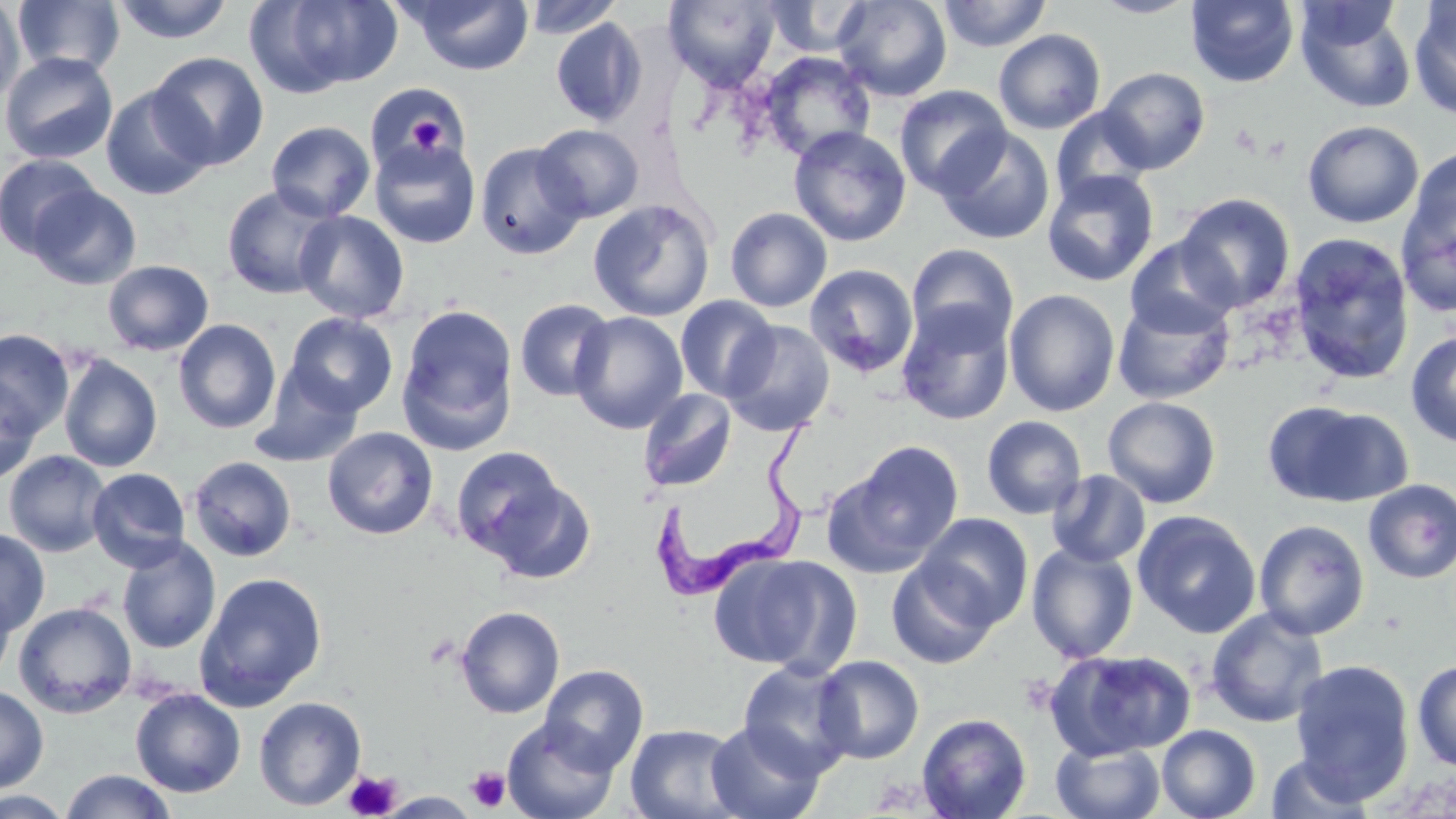

Approximate bounding boxes as (x1,y1)-(x2,y2) corner pairs in pixels. Uninfected red blood cell locations: (112,0)-(235,45), (248,0)-(403,95), (404,0)-(535,76), (522,0)-(623,39), (663,0)-(781,90), (763,0)-(874,58), (833,0)-(952,102), (937,0)-(1052,52), (1090,0)-(1198,18), (1186,0)-(1299,87), (0,1)-(26,106), (13,1)-(125,78), (1409,2)-(1456,121), (1295,3)-(1417,113), (550,17)-(648,127), (993,29)-(1106,134), (758,51)-(875,161), (0,52)-(119,165), (148,52)-(269,170), (1098,67)-(1210,174), (366,83)-(471,177), (100,84)-(214,200), (894,85)-(1012,199), (1051,107)-(1153,207), (1302,120)-(1424,229), (266,121)-(376,222), (533,124)-(644,222), (789,127)-(911,247), (936,127)-(1055,245), (369,139)-(481,249), (475,141)-(588,261), (1403,147)-(1456,259), (0,154)-(102,257), (1042,170)-(1160,287), (1397,180)-(1456,318), (28,184)-(141,289), (221,184)-(341,300), (1175,192)-(1296,312), (588,199)-(715,322), (724,207)-(833,312), (294,210)-(410,324), (1287,233)-(1414,385), (1124,236)-(1239,338), (906,243)-(1019,351), (102,259)-(214,356), (804,264)-(919,378), (1004,289)-(1120,417), (1112,294)-(1235,405), (674,295)-(779,402), (514,299)-(616,402), (896,303)-(1015,426), (396,304)-(519,453), (570,311)-(688,434), (285,312)-(398,416), (172,319)-(281,434), (722,320)-(835,436), (0,328)-(75,438), (1405,332)-(1456,448), (58,354)-(162,473), (250,368)-(364,469), (0,376)-(42,486), (637,388)-(736,493), (1102,396)-(1221,508), (1263,399)-(1413,509), (981,415)-(1087,520), (322,427)-(439,540), (824,441)-(964,578), (449,446)-(573,567), (3,450)-(112,557), (188,456)-(297,562), (86,468)-(191,571), (1047,470)-(1151,568), (1362,479)-(1456,584), (1132,510)-(1262,638), (916,513)-(1034,628), (1253,519)-(1370,640), (0,527)-(50,636), (116,537)-(221,654), (1026,542)-(1139,663), (709,551)-(860,675), (887,560)-(999,669), (193,571)-(328,711), (0,586)-(16,686), (13,601)-(137,718), (455,605)-(565,718), (1205,607)-(1328,728), (1044,649)-(1197,761), (813,655)-(924,764), (736,659)-(857,780), (1290,659)-(1415,802), (1412,659)-(1456,771), (539,664)-(649,774), (0,685)-(49,793), (130,688)-(246,798), (253,696)-(366,811), (916,713)-(1032,819), (502,718)-(620,819), (705,721)-(825,819), (625,723)-(745,819), (1156,724)-(1261,819), (1051,739)-(1166,819), (1264,751)-(1378,819), (59,769)-(178,819), (0,790)-(74,819). Trypanosoma brucei locations: (641,414)-(822,607). Platelet locations: (402,105)-(455,159), (466,766)-(510,812), (345,769)-(401,819). Slide-level diagnosis: Trypanosoma brucei. Optical microscopy. Thin blood film. Image is 1456×819 pixels. One field of a larger specimen. Captured at 1000x magnification. May-Grünwald-Giemsa stain.